Report the malaria status of this cell.
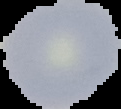
Uninfected.

From a thin blood film. The area outside the segmented cell region is set to black. Image is 121×109 pixels.